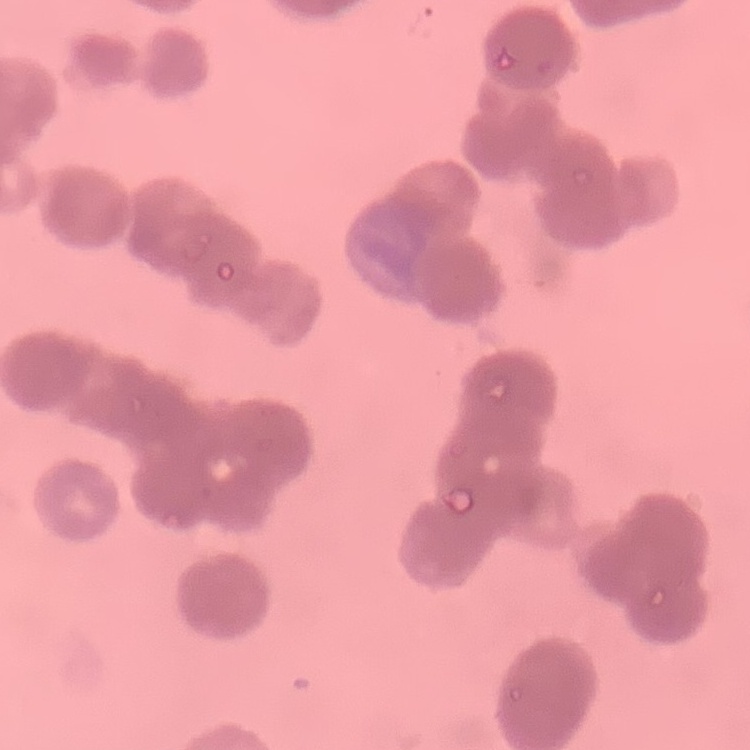

erythrocyte morphology = rouleaux formation
preparation = thin blood smear
image type = one tile cut from a larger photomicrograph
stain = Field's or Giemsa